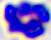
Summary:
  - Magnification: 400x
  - Modality: micrograph
  - Identification: leukocyte